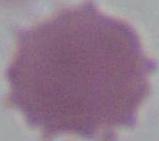
Summary:
  - Magnification: 1000x
  - Modality: micrograph
  - Identification: erythrocyte